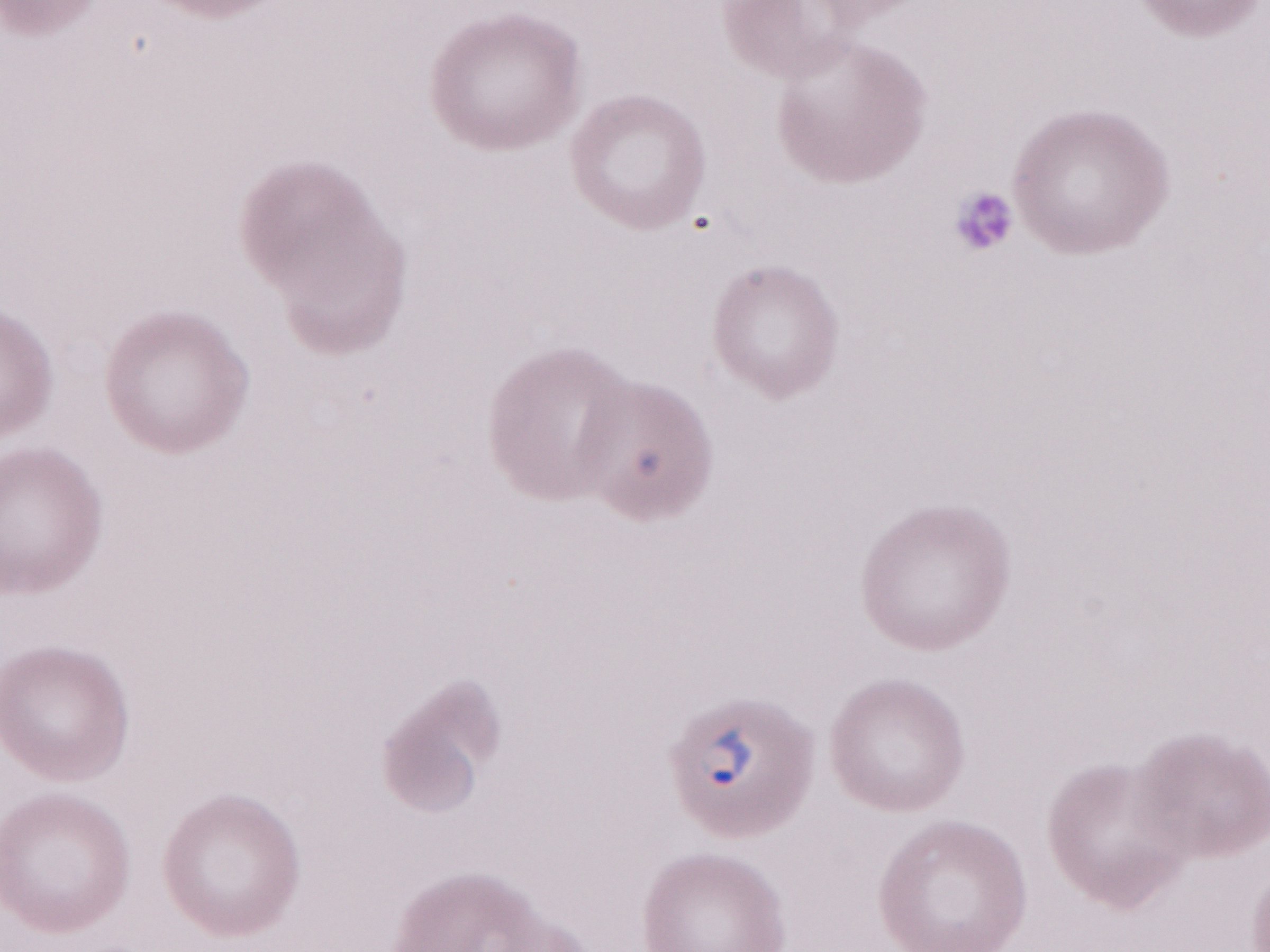 Thin blood film. Image is 1270×952 pixels. Olympus BX43 microscope and DP73 digital camera. May-Grünwald-Giemsa-stained preparation. 1,000x magnification. Patient diagnosis: malaria infection. One field of this slide.